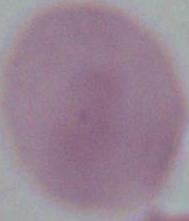
A red blood cell is shown. Captured at 1000x magnification. Micrograph.